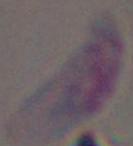 Captured at 1000x magnification. Micrograph. Toxoplasma gondii is seen.